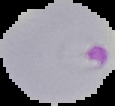

Image is 115×106 pixels. From a thin blood film. Segmented cell region on a black background. Result: Plasmodium parasites detected.